Assess this cell for malaria.
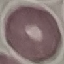

It is uninfected.

Cell patch, automatically extracted from a larger field of view and resized to 64 × 64 pixels. Giemsa stain. Thin blood film. Photographed with a smartphone camera at the microscope eyepiece.